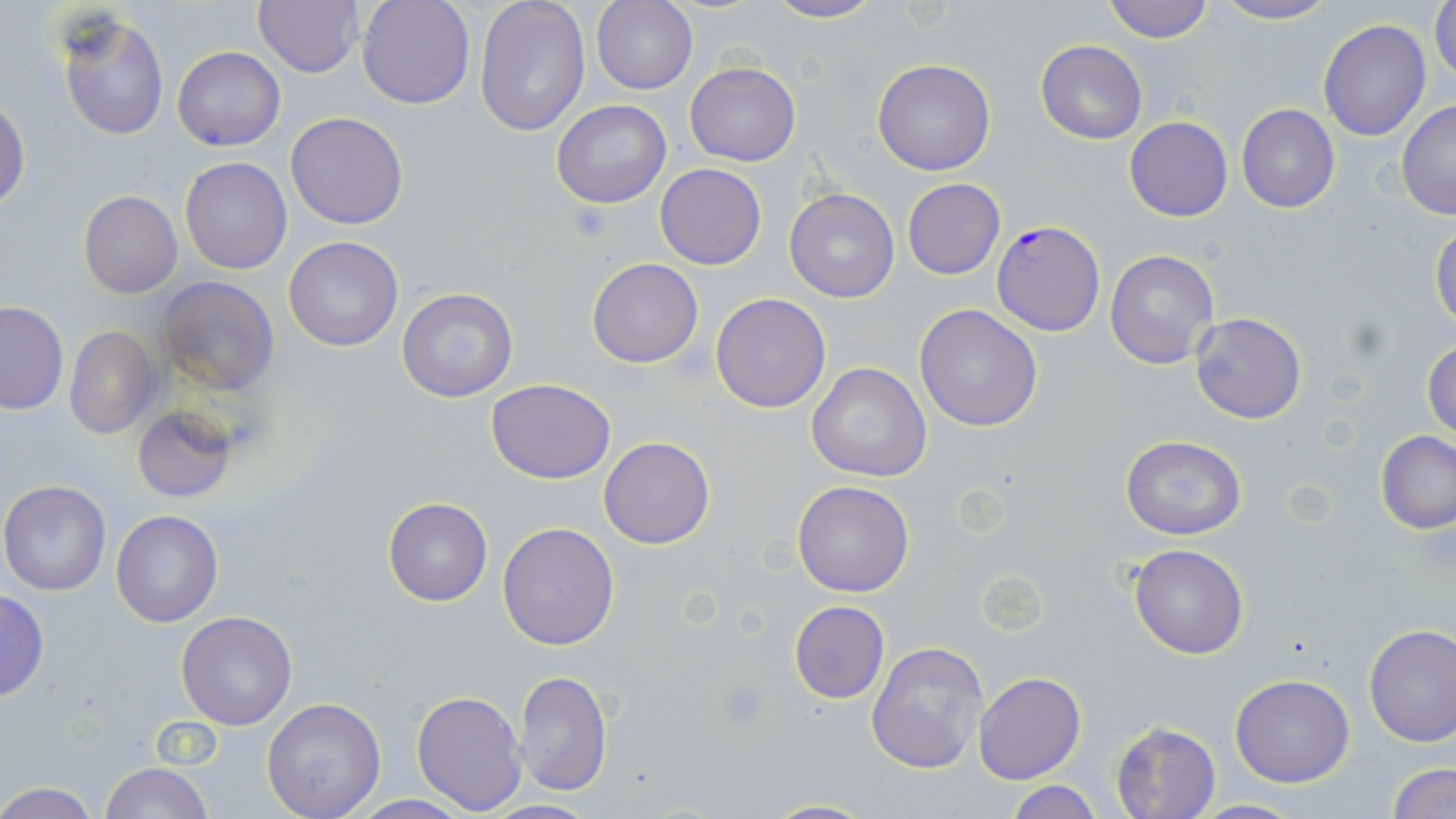

Summary:
  - Coordinate format: approximate bounding boxes as named x1/y1/x2/y2 corners in pixels
  - Plasmodium falciparum-infected red blood cell locations: (x1=993, y1=221, x2=1105, y2=336)
  - Uninfected red blood cell locations: (x1=357, y1=0, x2=474, y2=109), (x1=475, y1=0, x2=591, y2=139), (x1=762, y1=0, x2=884, y2=24), (x1=1101, y1=0, x2=1216, y2=43), (x1=1431, y1=0, x2=1456, y2=88), (x1=252, y1=1, x2=365, y2=78), (x1=592, y1=1, x2=698, y2=95), (x1=1210, y1=1, x2=1336, y2=25), (x1=56, y1=12, x2=170, y2=141), (x1=1318, y1=18, x2=1432, y2=140), (x1=1036, y1=40, x2=1146, y2=146), (x1=172, y1=46, x2=285, y2=150), (x1=873, y1=59, x2=995, y2=176), (x1=685, y1=63, x2=800, y2=166), (x1=0, y1=97, x2=29, y2=213), (x1=551, y1=100, x2=671, y2=208), (x1=1396, y1=101, x2=1456, y2=219), (x1=1236, y1=104, x2=1340, y2=214), (x1=286, y1=110, x2=409, y2=230), (x1=1124, y1=118, x2=1234, y2=221), (x1=178, y1=157, x2=293, y2=275), (x1=655, y1=163, x2=766, y2=269), (x1=901, y1=179, x2=1005, y2=279), (x1=785, y1=188, x2=900, y2=303), (x1=78, y1=190, x2=183, y2=299), (x1=1429, y1=222, x2=1456, y2=331), (x1=283, y1=236, x2=403, y2=351), (x1=1104, y1=248, x2=1219, y2=370), (x1=586, y1=259, x2=705, y2=368), (x1=155, y1=275, x2=281, y2=397), (x1=397, y1=286, x2=518, y2=404), (x1=710, y1=293, x2=831, y2=412), (x1=0, y1=302, x2=69, y2=414), (x1=913, y1=303, x2=1042, y2=432), (x1=1189, y1=312, x2=1306, y2=423), (x1=64, y1=325, x2=161, y2=440), (x1=1422, y1=338, x2=1455, y2=440), (x1=805, y1=362, x2=931, y2=483), (x1=486, y1=379, x2=616, y2=484), (x1=133, y1=405, x2=238, y2=504), (x1=1376, y1=431, x2=1456, y2=535), (x1=1121, y1=434, x2=1247, y2=541), (x1=599, y1=437, x2=715, y2=549), (x1=0, y1=480, x2=111, y2=596), (x1=792, y1=480, x2=914, y2=597), (x1=383, y1=498, x2=493, y2=605), (x1=112, y1=510, x2=224, y2=627), (x1=496, y1=522, x2=619, y2=650), (x1=1128, y1=543, x2=1249, y2=660), (x1=0, y1=589, x2=49, y2=702), (x1=788, y1=601, x2=889, y2=704), (x1=176, y1=609, x2=299, y2=730), (x1=1364, y1=624, x2=1456, y2=748), (x1=866, y1=639, x2=988, y2=774), (x1=514, y1=670, x2=612, y2=796), (x1=974, y1=673, x2=1086, y2=785), (x1=1230, y1=675, x2=1356, y2=788), (x1=410, y1=688, x2=526, y2=815), (x1=261, y1=698, x2=386, y2=818), (x1=1110, y1=722, x2=1221, y2=819), (x1=101, y1=761, x2=214, y2=819), (x1=1386, y1=763, x2=1454, y2=819), (x1=1000, y1=780, x2=1103, y2=818), (x1=0, y1=784, x2=98, y2=818), (x1=755, y1=798, x2=878, y2=818), (x1=1186, y1=798, x2=1310, y2=817), (x1=483, y1=799, x2=599, y2=817)
  - Platelet locations: (x1=566, y1=201, x2=613, y2=245)
  - Slide-level diagnosis: Plasmodium falciparum
  - Magnification: 1000x
  - Modality: optical microscopy
  - Preparation: thin blood film
  - Image size: 1456×819 pixels
  - Stain: May-Grünwald-Giemsa
  - Field of view: single